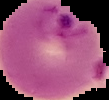
Summary:
  - Preparation: thin blood smear
  - Malaria status: parasitized
  - Image type: segmented cell region with the area outside set to black
  - Image size: 109×100 pixels